Locate every blood parasite and identify its species.
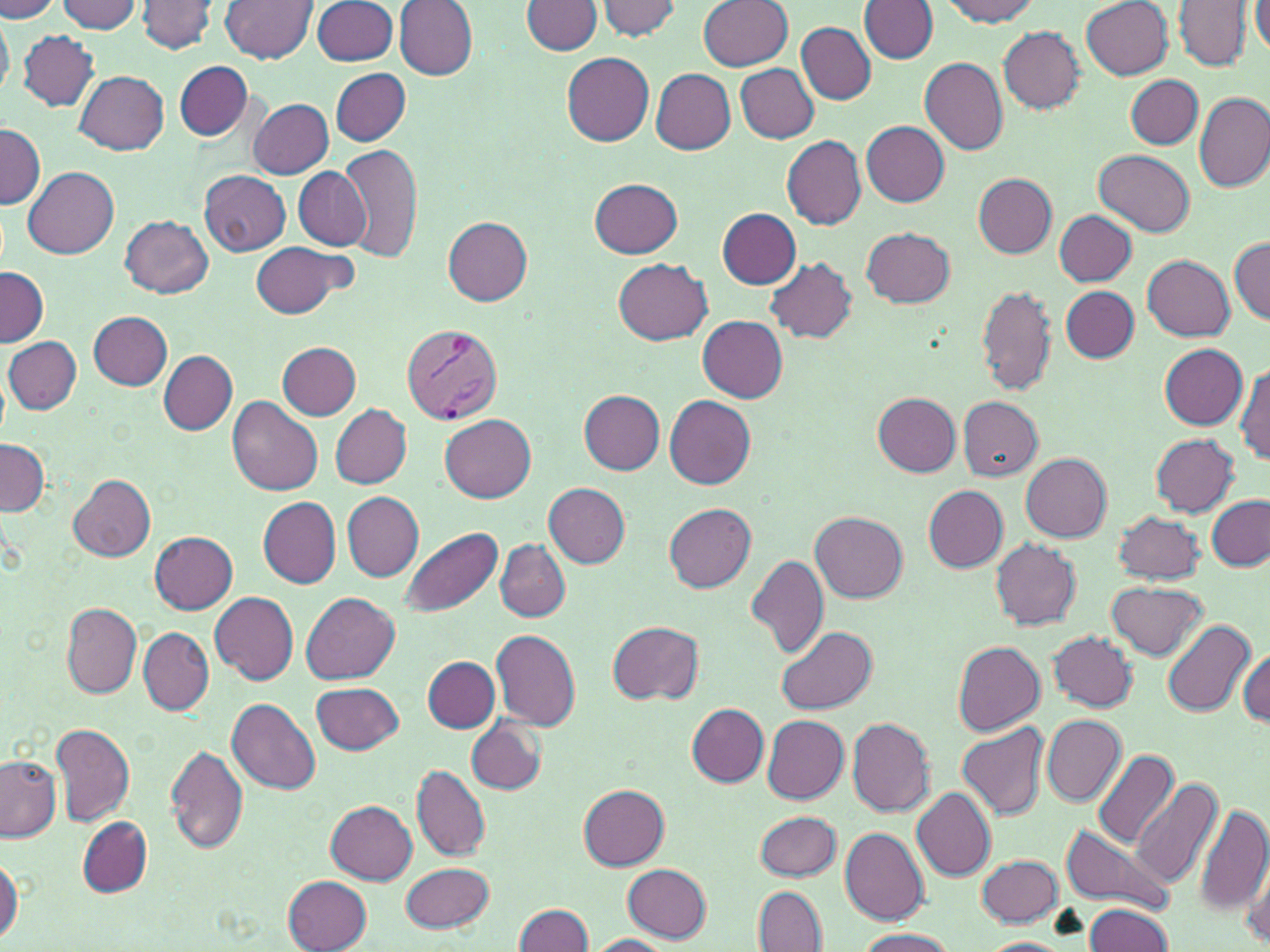
Approximate bounding boxes as (x1,y1)-(x2,y2) corner pairs in pixels.
Plasmodium vivax-infected red blood cells: (401,323)-(502,426).
No Plasmodium falciparum, Plasmodium ovale, Plasmodium malariae, Babesia divergens, or Trypanosoma brucei observed.

{
  "slide_level_diagnosis": "Plasmodium vivax",
  "stain": "May-Grünwald-Giemsa",
  "image_size": "1270×952 pixels",
  "magnification": "1000x",
  "preparation": "thin blood film",
  "modality": "optical microscopy",
  "uninfected_red_blood_cell_locations": "approximate bounding boxes as (x1,y1)-(x2,y2) corner pairs in pixels: (596,0)-(683,41), (698,0)-(792,70), (941,0)-(1041,25), (1081,0)-(1173,79), (1249,0)-(1270,58), (0,1)-(61,21), (55,1)-(141,33), (137,1)-(218,54), (220,1)-(317,62), (312,1)-(397,66), (522,1)-(602,56), (1174,1)-(1251,70), (394,2)-(478,79), (862,2)-(939,63), (0,10)-(13,101), (797,23)-(875,104), (998,27)-(1085,113), (18,29)-(99,112), (562,53)-(654,146), (919,57)-(1007,154), (174,60)-(253,141), (735,63)-(819,142), (650,68)-(735,154), (331,69)-(410,145), (75,70)-(168,154), (1126,75)-(1203,149), (1194,91)-(1270,191), (249,98)-(334,179), (861,121)-(949,207), (0,123)-(43,209), (780,136)-(866,228), (341,142)-(423,262), (1094,150)-(1196,238), (24,166)-(119,259), (293,167)-(372,251), (200,170)-(291,255), (972,174)-(1057,257), (589,178)-(684,258), (717,208)-(800,288), (1055,210)-(1137,286), (121,217)-(213,298), (443,217)-(532,305), (862,228)-(955,308), (1231,237)-(1269,324), (250,242)-(352,318), (1142,255)-(1234,340), (614,258)-(712,344), (766,258)-(856,342), (0,267)-(48,348), (976,284)-(1057,397), (1061,285)-(1138,362), (89,312)-(172,389), (697,315)-(787,401), (4,336)-(81,414), (278,342)-(361,420), (1159,344)-(1248,429), (159,351)-(237,435), (1235,365)-(1269,467), (580,391)-(664,474), (873,392)-(961,477), (664,395)-(756,488), (227,397)-(323,498), (957,397)-(1043,480), (331,405)-(411,488), (440,413)-(537,502), (1151,434)-(1240,517), (0,439)-(48,517), (1021,453)-(1112,542), (68,474)-(156,561), (544,483)-(630,567), (922,485)-(1009,572), (343,492)-(424,580), (258,497)-(341,589), (1206,497)-(1270,571), (664,503)-(756,592), (810,511)-(908,603), (1112,511)-(1205,585), (400,527)-(502,618), (150,531)-(239,613), (991,538)-(1081,629), (496,539)-(570,622), (746,554)-(830,659), (1107,581)-(1208,659), (209,591)-(299,685), (300,592)-(400,684), (62,603)-(141,698), (608,620)-(704,704), (1161,620)-(1255,717), (774,625)-(875,713), (139,628)-(214,715), (491,628)-(582,730), (1048,631)-(1137,712), (951,640)-(1045,735), (1240,649)-(1270,727), (423,657)-(499,732), (311,684)-(404,753), (227,697)-(322,796), (686,702)-(769,785), (762,714)-(848,803), (1042,715)-(1126,805), (467,716)-(546,795), (847,717)-(935,815), (957,722)-(1049,822), (50,723)-(135,827), (166,745)-(247,854), (1091,747)-(1180,848), (0,757)-(60,843), (412,765)-(491,862), (1132,777)-(1223,889), (578,785)-(669,869), (912,787)-(995,880), (326,800)-(418,884), (1195,801)-(1270,921), (755,810)-(842,881), (78,818)-(153,895), (1059,822)-(1174,915), (840,826)-(929,927), (1237,844)-(1270,945), (0,854)-(23,946), (977,855)-(1063,926), (402,863)-(496,931), (622,864)-(713,942), (283,875)-(371,952), (754,886)-(828,952), (1083,903)-(1176,952), (513,904)-(594,952), (854,927)-(955,952), (584,935)-(675,951), (979,937)-(1071,951)",
  "field_of_view": "single"
}